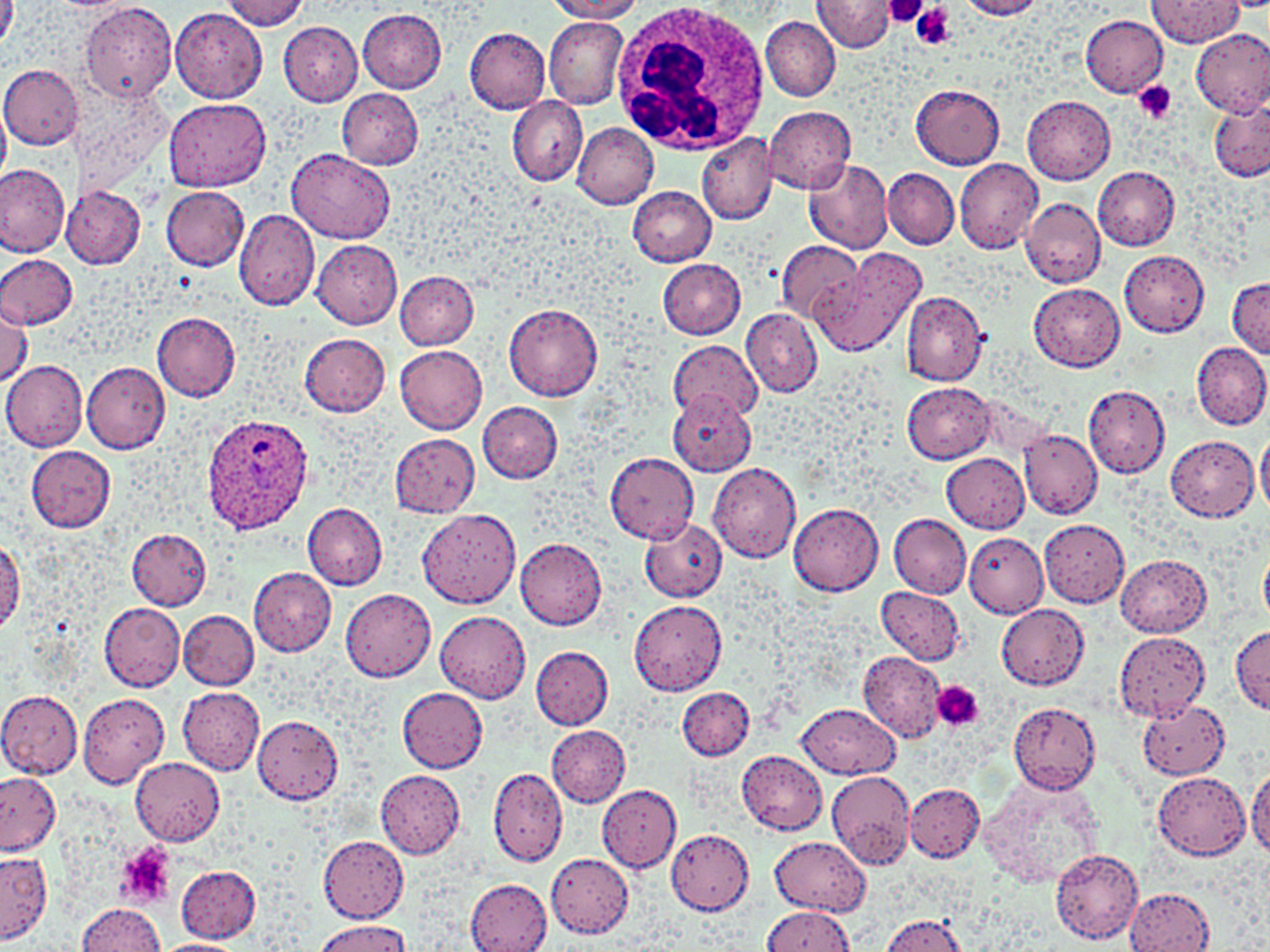
Approximate bounding boxes as [x1, y1, x2, y2] in pixels. Platelet locations: [882, 0, 930, 26], [911, 4, 956, 51], [1133, 81, 1177, 126], [932, 682, 983, 732], [117, 843, 176, 909]. Uninfected red blood cell locations: [0, 0, 20, 55], [223, 0, 308, 30], [546, 0, 644, 21], [956, 0, 1048, 19], [1147, 0, 1243, 47], [813, 1, 897, 51], [79, 3, 178, 105], [170, 8, 267, 103], [358, 9, 447, 93], [1079, 15, 1168, 97], [761, 16, 841, 100], [544, 17, 627, 109], [279, 22, 364, 105], [464, 28, 551, 113], [1192, 28, 1270, 117], [0, 63, 83, 150], [911, 85, 1005, 168], [338, 90, 425, 168], [1022, 93, 1115, 185], [506, 95, 588, 186], [1210, 96, 1270, 183], [162, 98, 271, 192], [0, 106, 10, 186], [765, 107, 856, 195], [572, 121, 659, 209], [696, 132, 777, 227], [287, 149, 396, 244], [803, 156, 894, 255], [954, 159, 1043, 254], [0, 162, 70, 257], [1093, 167, 1180, 250], [884, 168, 958, 250], [61, 186, 146, 268], [161, 186, 249, 270], [628, 187, 717, 267], [1021, 196, 1105, 288], [234, 210, 320, 311], [311, 238, 403, 327], [775, 240, 863, 324], [811, 248, 924, 357], [1120, 250, 1210, 336], [0, 254, 77, 328], [658, 258, 747, 340], [395, 271, 479, 350], [1227, 277, 1270, 358], [1028, 283, 1125, 372], [900, 291, 988, 386], [0, 303, 32, 387], [504, 304, 604, 401], [742, 308, 822, 397], [152, 312, 241, 400], [299, 333, 390, 416], [669, 340, 762, 422], [1190, 342, 1270, 431], [394, 344, 488, 434], [1, 359, 88, 452], [81, 361, 169, 453], [902, 382, 995, 462], [1081, 383, 1170, 479], [667, 389, 756, 477], [477, 401, 563, 483], [1018, 429, 1101, 519], [1257, 429, 1270, 517], [390, 432, 481, 516], [1166, 436, 1259, 522], [25, 445, 116, 532], [605, 451, 698, 544], [943, 453, 1030, 533], [708, 462, 802, 564], [788, 502, 884, 596], [303, 503, 388, 589], [418, 509, 523, 610], [888, 513, 971, 598], [638, 517, 726, 602], [1040, 519, 1130, 607], [126, 527, 212, 609], [963, 534, 1047, 617], [514, 536, 607, 630], [0, 537, 24, 632], [1259, 540, 1270, 629], [1117, 554, 1211, 637], [248, 566, 336, 655], [876, 585, 965, 667], [341, 588, 436, 680], [629, 597, 727, 696], [98, 602, 186, 692], [996, 604, 1090, 689], [179, 610, 258, 689], [436, 610, 532, 703], [1230, 628, 1270, 714], [1114, 631, 1210, 722], [531, 646, 613, 730], [859, 653, 945, 742], [178, 687, 265, 774], [397, 687, 487, 772], [677, 687, 754, 760], [0, 690, 84, 778], [77, 693, 169, 787], [1137, 700, 1230, 779], [1007, 701, 1100, 794], [798, 703, 900, 778], [252, 716, 344, 803], [547, 726, 629, 806], [737, 751, 827, 835], [132, 757, 224, 845], [488, 766, 568, 867], [1246, 766, 1270, 858], [375, 770, 465, 860], [826, 770, 914, 870], [0, 771, 61, 856], [1152, 771, 1251, 859], [978, 775, 1107, 892], [903, 782, 985, 862], [597, 785, 681, 872], [666, 827, 754, 915], [316, 835, 409, 923], [770, 837, 869, 915], [1050, 847, 1144, 943], [0, 851, 51, 943], [547, 853, 633, 936], [176, 864, 260, 942], [465, 879, 551, 951], [1124, 888, 1214, 951], [77, 902, 165, 952], [761, 907, 853, 952], [879, 914, 969, 952], [314, 919, 408, 952], [153, 938, 249, 952]. Plasmodium ovale-infected red blood cell locations: [201, 413, 313, 533]. White blood cell locations: [611, 0, 772, 155]. Slide-level diagnosis: Plasmodium ovale. Thin blood film. May-Grünwald-Giemsa stain. Light microscopy. Image is 1270×952 pixels. Captured at 1000x magnification. Single field of view.